Assess the morphology of the red blood cells.
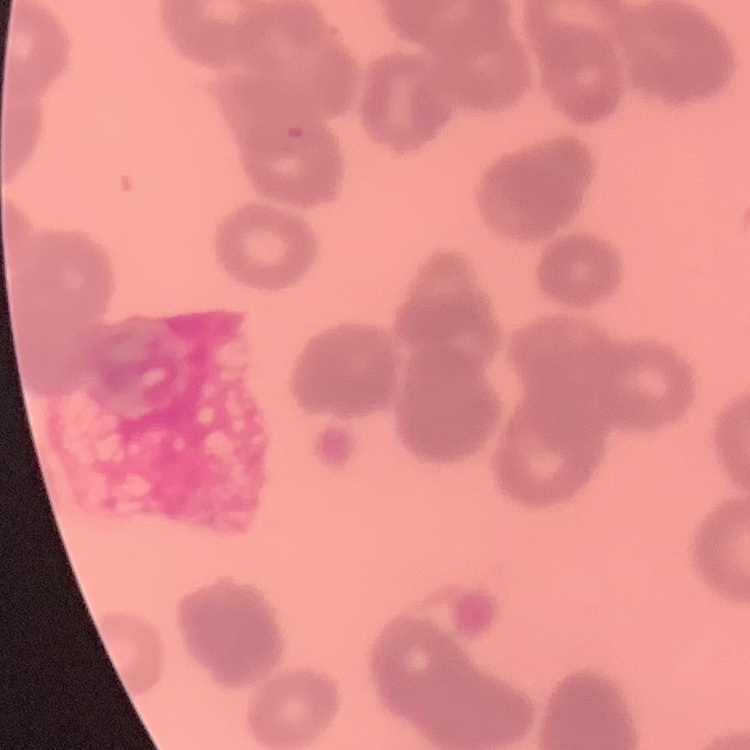
Rouleaux formation.

Summary:
  - Preparation: thin blood smear
  - Stain: Field's or Giemsa
  - Image type: square crop of a larger photomicrograph